Assess this cell for malaria.
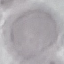
It is uninfected.

Automatically extracted cell patch, resized to 64 × 64 pixels. Acquired by smartphone through the microscope eyepiece. Thin blood smear. Giemsa stain.